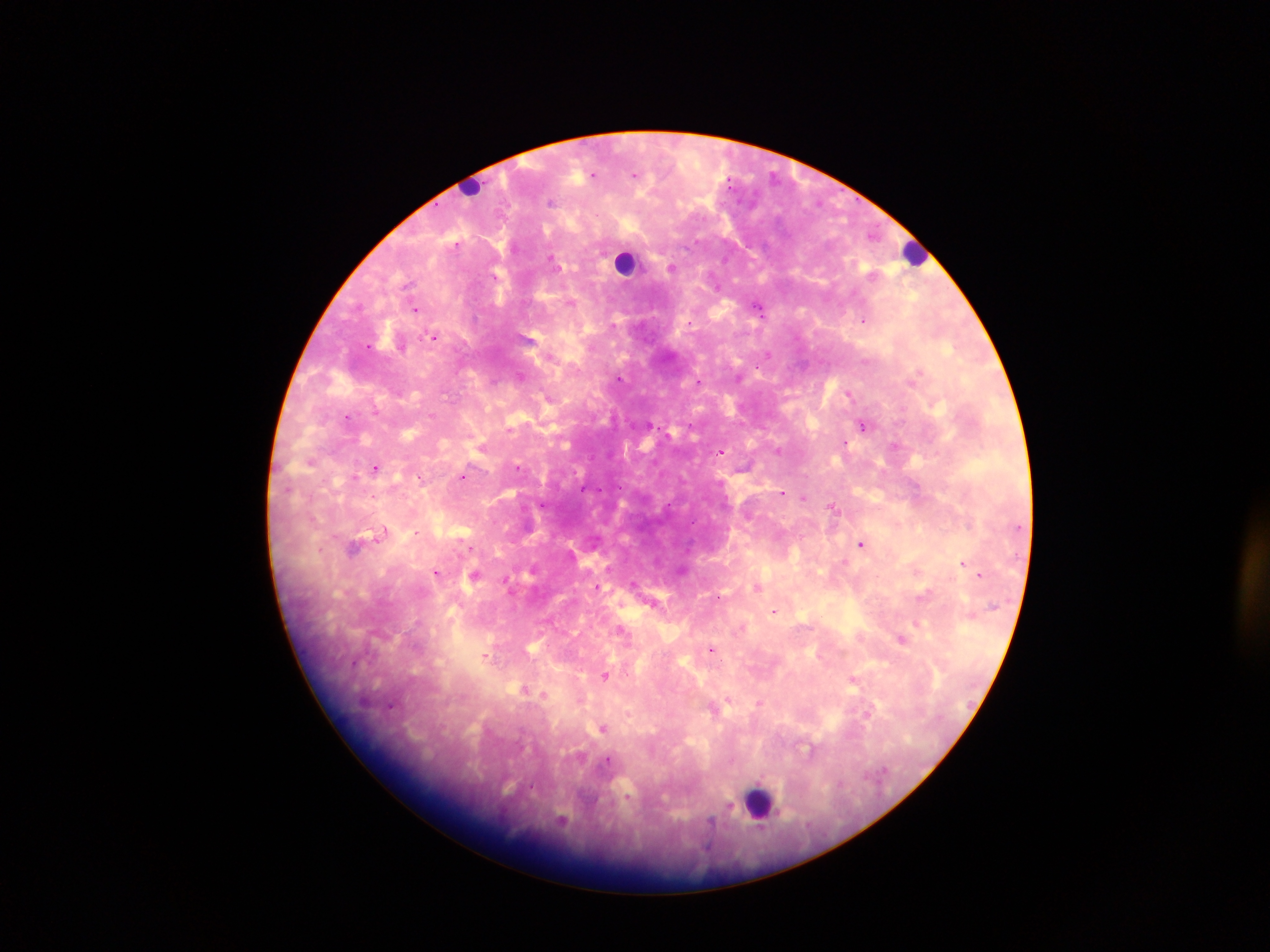

Approximate centers as (x, y) in pixels. Leukocyte locations: (468, 193), (917, 253), (624, 266), (760, 799). Plasmodium parasite locations: (593, 174), (774, 175), (551, 202), (555, 261), (672, 267), (570, 305), (758, 306), (416, 307), (864, 321), (434, 337), (530, 338), (367, 344), (766, 356), (521, 376), (620, 376), (738, 379), (700, 382), (502, 383), (851, 391), (449, 395), (547, 398), (552, 402), (376, 410), (613, 414), (348, 418), (650, 424), (513, 426), (864, 426), (846, 442), (894, 445), (481, 448), (778, 448), (721, 451), (311, 464), (520, 467), (376, 469), (463, 476), (355, 477), (782, 493), (804, 496), (833, 506), (356, 544), (861, 544), (961, 563), (531, 570), (915, 572), (436, 573), (979, 574), (757, 588), (773, 613), (918, 623), (623, 633), (901, 640), (532, 648), (711, 648), (487, 654), (607, 675), (852, 679), (523, 690), (544, 694), (759, 703), (712, 709), (869, 716), (604, 726), (808, 749), (627, 793), (563, 820). Mobile-phone photograph taken through the microscope. Collected in Ghana. Thick blood film. Image is 1270×952 pixels. Single field of view.